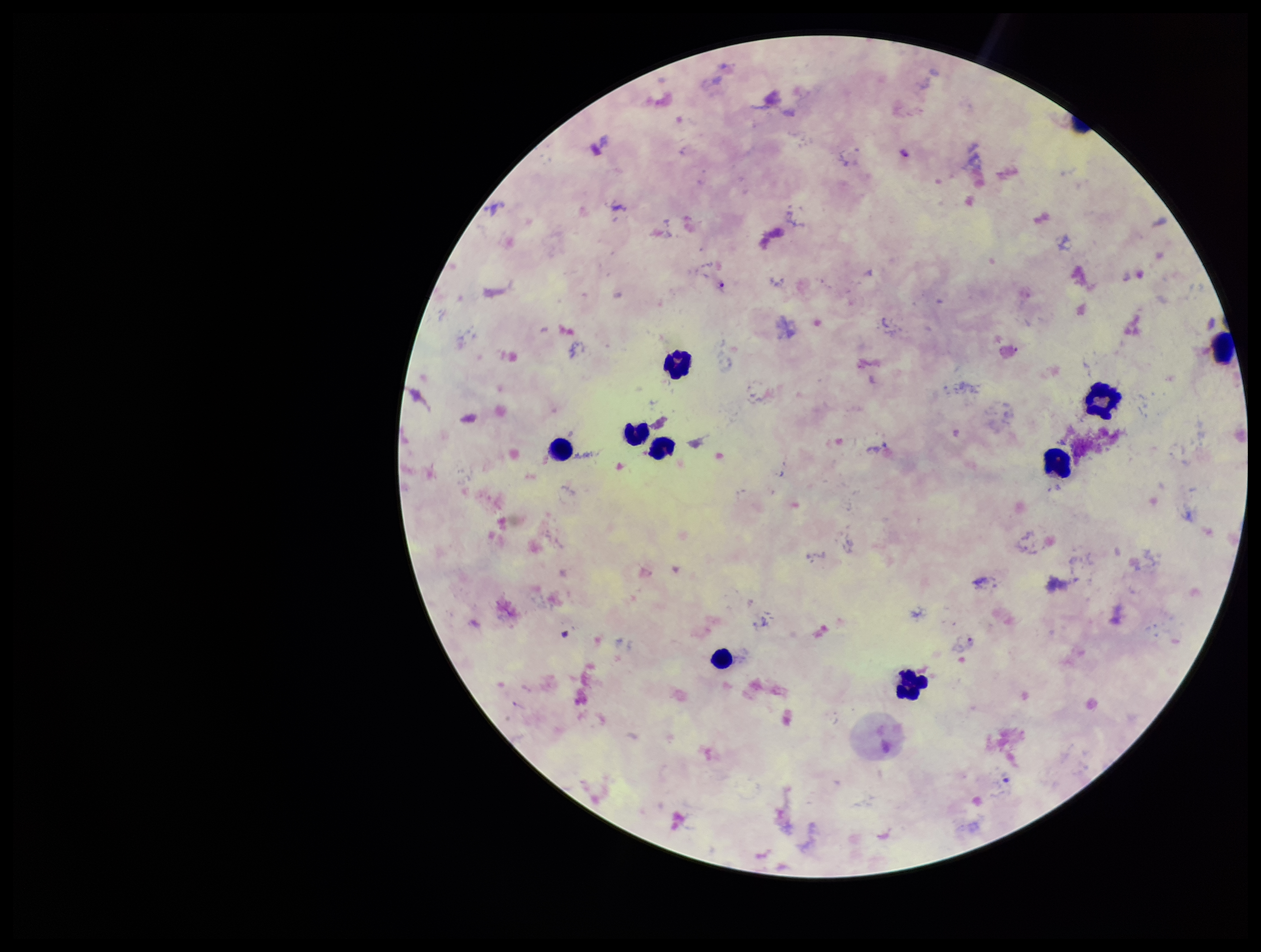
Summary:
  - Preparation: thick smear
  - Species reported for this patient: Plasmodium falciparum
  - Plasmodium parasites: detected
  - Field of view: one from this slide
  - Patient malaria status: infected
  - Capture: smartphone photograph through the microscope eyepiece
  - Stain: Giemsa
  - Leukocyte count: 9
  - Parasite count: 4
  - Image size: 1261×952 pixels